Assess the morphology of the red blood cells.
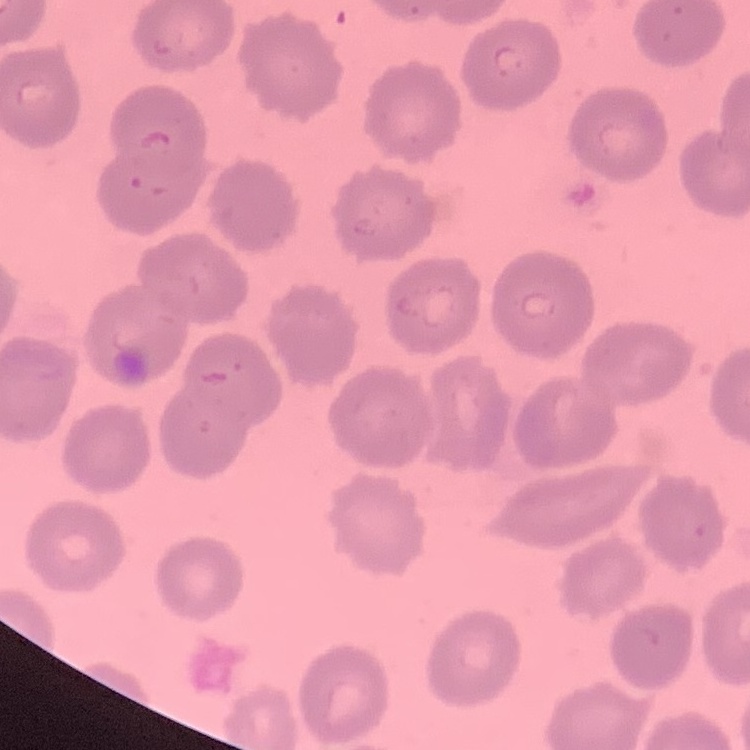
No rouleaux formation.

{
  "stain": "Field's or Giemsa",
  "preparation": "thin peripheral smear",
  "image_type": "one tile cut from a larger photomicrograph"
}